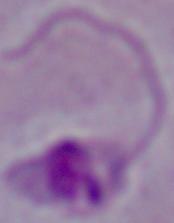

Captured at 1000x magnification. Micrograph. A Leishmania parasite is shown.